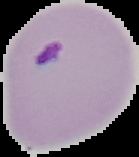
image_size: 139×157 pixels
image_type: cell region segmented out of the field of view; surrounding area masked to black
preparation: thin blood smear
result: Plasmodium parasites detected